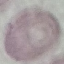
Result: no malaria parasites seen. Cell patch, automatically extracted from a larger field of view and resized to 64 × 64 pixels. Thin blood film. Giemsa stain. Photographed with a smartphone camera at the microscope eyepiece.